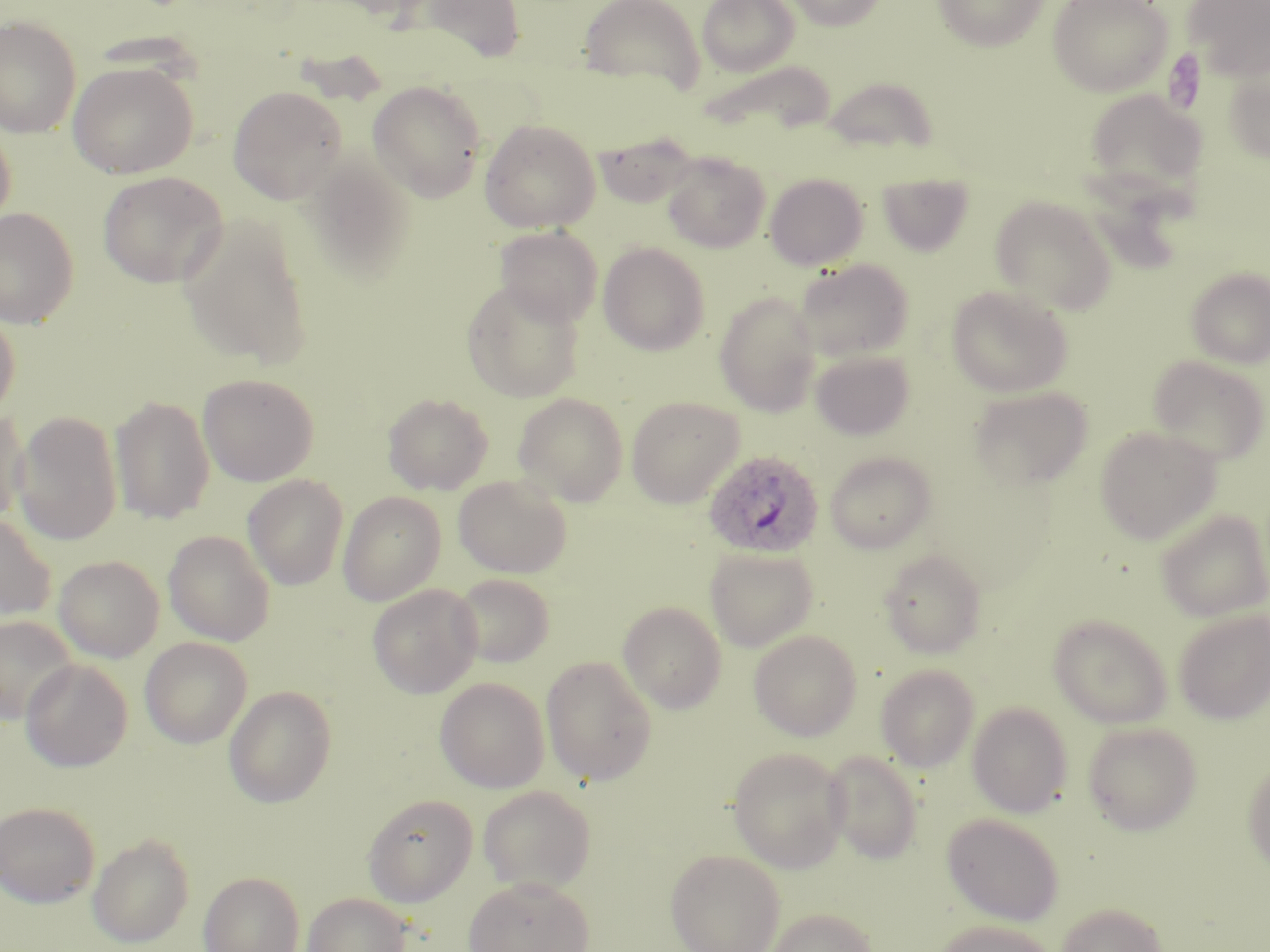

Approximate bounding boxes as (x1, y1, x2, y2) in pixels. Plasmodium ovale-infected red blood cell locations: (704, 450, 825, 560). Uninfected red blood cell locations: (314, 0, 435, 18), (414, 0, 527, 63), (578, 0, 706, 93), (696, 0, 799, 77), (787, 0, 886, 31), (933, 0, 1049, 50), (1182, 0, 1270, 83), (1047, 1, 1173, 97), (0, 15, 82, 138), (68, 61, 198, 179), (696, 61, 833, 136), (1223, 65, 1270, 163), (824, 76, 940, 156), (367, 81, 486, 202), (228, 86, 347, 204), (1084, 88, 1207, 204), (0, 117, 16, 235), (479, 119, 601, 233), (592, 131, 699, 209), (662, 152, 770, 253), (303, 155, 418, 282), (98, 171, 228, 287), (877, 172, 975, 256), (765, 173, 868, 271), (990, 196, 1116, 314), (0, 207, 79, 329), (178, 214, 314, 368), (495, 226, 603, 328), (598, 242, 710, 355), (793, 259, 914, 362), (1185, 267, 1270, 369), (462, 280, 585, 402), (947, 285, 1072, 398), (714, 291, 822, 417), (0, 308, 20, 421), (810, 349, 915, 440), (1148, 355, 1269, 465), (198, 373, 319, 486), (969, 385, 1093, 490), (383, 392, 493, 495), (513, 392, 629, 506), (109, 395, 216, 524), (626, 395, 743, 508), (0, 408, 30, 525), (13, 410, 123, 546), (1094, 426, 1221, 545), (825, 451, 937, 554), (243, 475, 348, 590), (453, 475, 572, 578), (338, 491, 446, 605), (1155, 508, 1270, 622), (0, 511, 55, 626), (163, 529, 276, 646), (705, 548, 818, 652), (879, 549, 986, 658), (53, 554, 164, 662), (450, 573, 556, 668), (367, 583, 482, 698), (618, 600, 727, 713), (1174, 610, 1270, 724), (1048, 614, 1172, 728), (0, 615, 78, 725), (748, 629, 862, 741), (140, 637, 252, 749), (540, 655, 658, 785), (20, 659, 133, 772), (876, 664, 979, 772), (434, 677, 550, 793), (223, 685, 337, 808), (967, 701, 1073, 818), (1082, 721, 1202, 835), (728, 747, 848, 873), (823, 751, 923, 864), (1243, 758, 1270, 875), (478, 786, 597, 895), (363, 794, 479, 907), (0, 802, 99, 906), (942, 813, 1065, 925), (87, 833, 195, 948), (666, 848, 785, 952), (199, 871, 305, 952), (464, 876, 594, 952), (302, 892, 412, 952), (1056, 902, 1168, 952), (766, 907, 876, 952), (931, 919, 1055, 952). Slide-level diagnosis: Plasmodium ovale. Thin blood smear. Captured at 1000x magnification. Image is 1270×952 pixels. Light microscopy. May-Grünwald-Giemsa-stained preparation. Single field of view.